Name the blood parasite species.
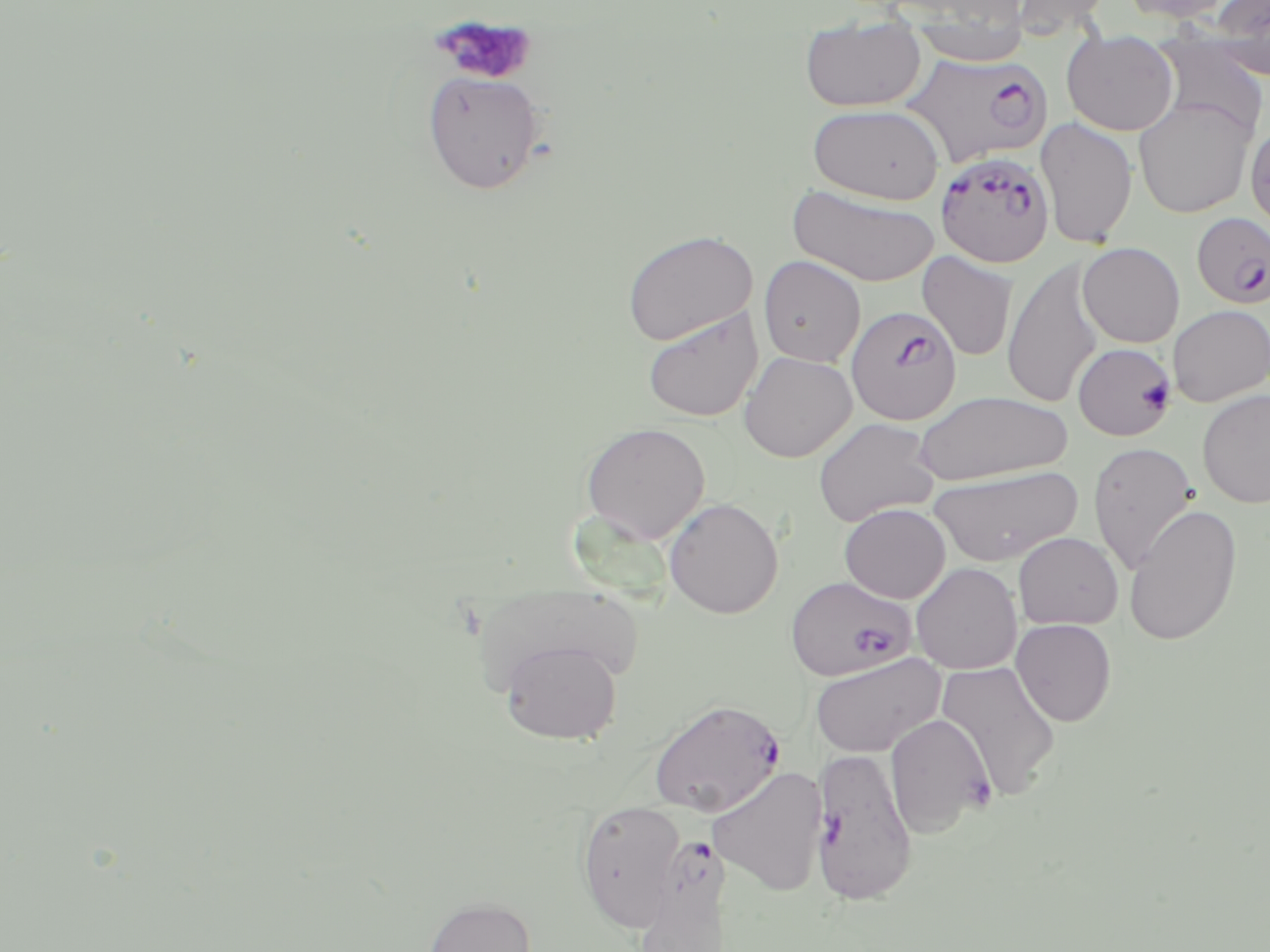

Plasmodium falciparum.

Summary:
  - Coordinate format: approximate bounding boxes as named x1/y1/x2/y2 corners in pixels
  - Plasmodium falciparum-infected red blood cell locations: (x1=901, y1=52, x2=1051, y2=169), (x1=936, y1=152, x2=1055, y2=268), (x1=1191, y1=212, x2=1270, y2=309), (x1=846, y1=304, x2=961, y2=425), (x1=1072, y1=342, x2=1177, y2=441), (x1=786, y1=575, x2=916, y2=680), (x1=648, y1=698, x2=785, y2=817), (x1=811, y1=746, x2=919, y2=905), (x1=641, y1=837, x2=732, y2=952)
  - Uninfected red blood cell locations: (x1=1009, y1=0, x2=1112, y2=38), (x1=1118, y1=0, x2=1237, y2=24), (x1=1209, y1=1, x2=1269, y2=81), (x1=909, y1=13, x2=1029, y2=66), (x1=799, y1=17, x2=927, y2=112), (x1=1061, y1=29, x2=1180, y2=136), (x1=1151, y1=34, x2=1268, y2=140), (x1=421, y1=70, x2=545, y2=194), (x1=1133, y1=97, x2=1255, y2=218), (x1=808, y1=104, x2=944, y2=204), (x1=1036, y1=116, x2=1138, y2=249), (x1=787, y1=183, x2=940, y2=287), (x1=621, y1=229, x2=758, y2=346), (x1=1077, y1=242, x2=1185, y2=348), (x1=917, y1=251, x2=1018, y2=361), (x1=757, y1=255, x2=866, y2=367), (x1=1003, y1=259, x2=1104, y2=408), (x1=1167, y1=305, x2=1270, y2=406), (x1=642, y1=308, x2=762, y2=422), (x1=739, y1=351, x2=857, y2=463), (x1=1197, y1=389, x2=1270, y2=509), (x1=914, y1=391, x2=1073, y2=485), (x1=812, y1=416, x2=941, y2=528), (x1=580, y1=422, x2=710, y2=544), (x1=1088, y1=441, x2=1200, y2=574), (x1=927, y1=465, x2=1081, y2=566), (x1=664, y1=498, x2=784, y2=619), (x1=839, y1=503, x2=951, y2=603), (x1=1123, y1=503, x2=1243, y2=647), (x1=1013, y1=532, x2=1123, y2=630), (x1=910, y1=562, x2=1022, y2=674), (x1=1011, y1=618, x2=1117, y2=726), (x1=500, y1=640, x2=623, y2=745), (x1=809, y1=653, x2=944, y2=758), (x1=936, y1=660, x2=1061, y2=801), (x1=884, y1=714, x2=993, y2=837), (x1=708, y1=765, x2=828, y2=896), (x1=576, y1=801, x2=688, y2=932), (x1=424, y1=896, x2=536, y2=952)
  - Platelet locations: (x1=434, y1=15, x2=537, y2=85)
  - Preparation: thin blood smear
  - Field of view: single
  - Image size: 1270×952 pixels
  - Stain: May-Grünwald-Giemsa
  - Modality: optical microscopy
  - Magnification: 1000x